Evaluate for malaria.
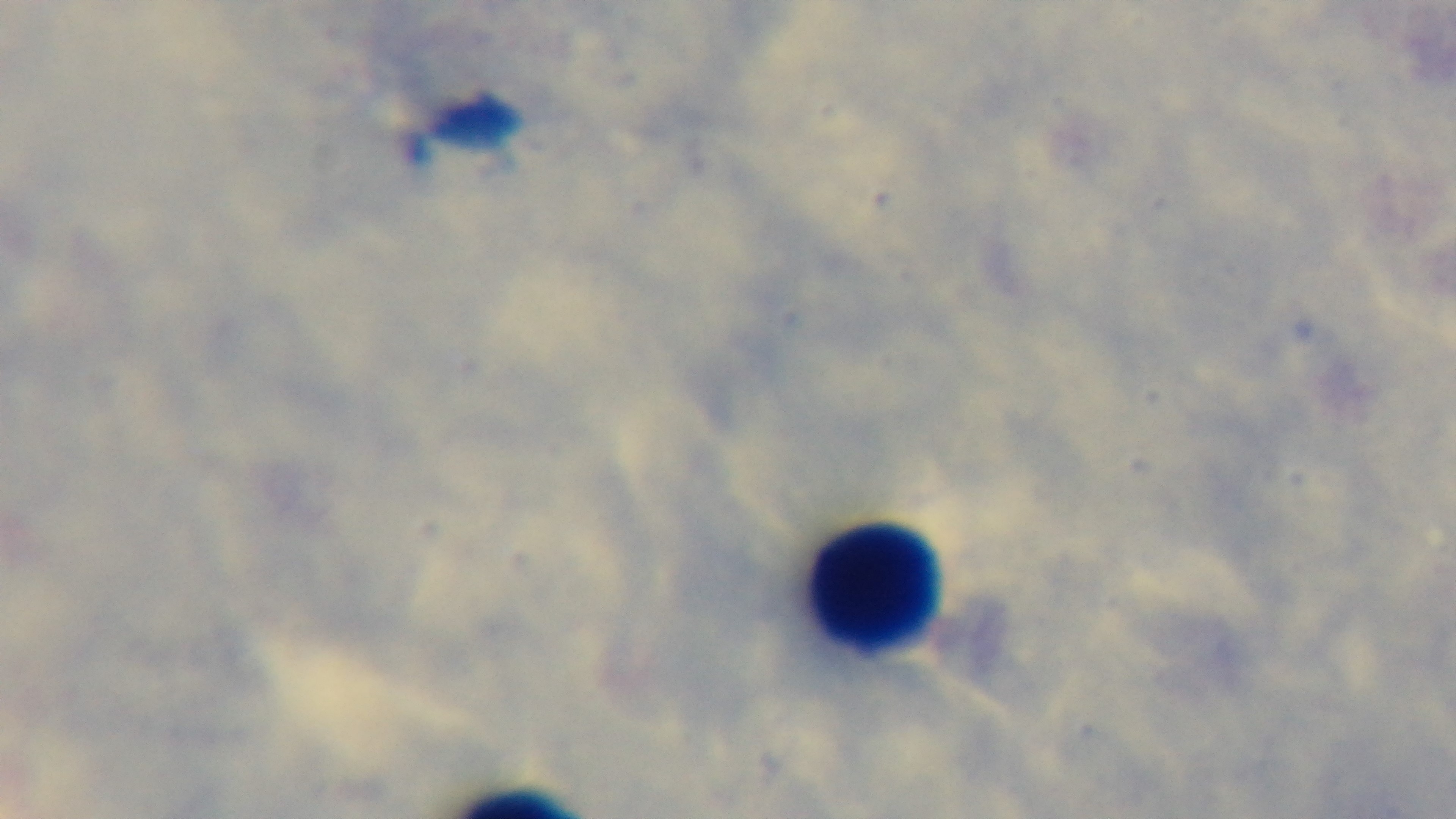

Uninfected.

stain = Giemsa
modality = light microscopy
capture = mounted 4K digital camera
preparation = thick
objective = 100x oil immersion
field of view = single